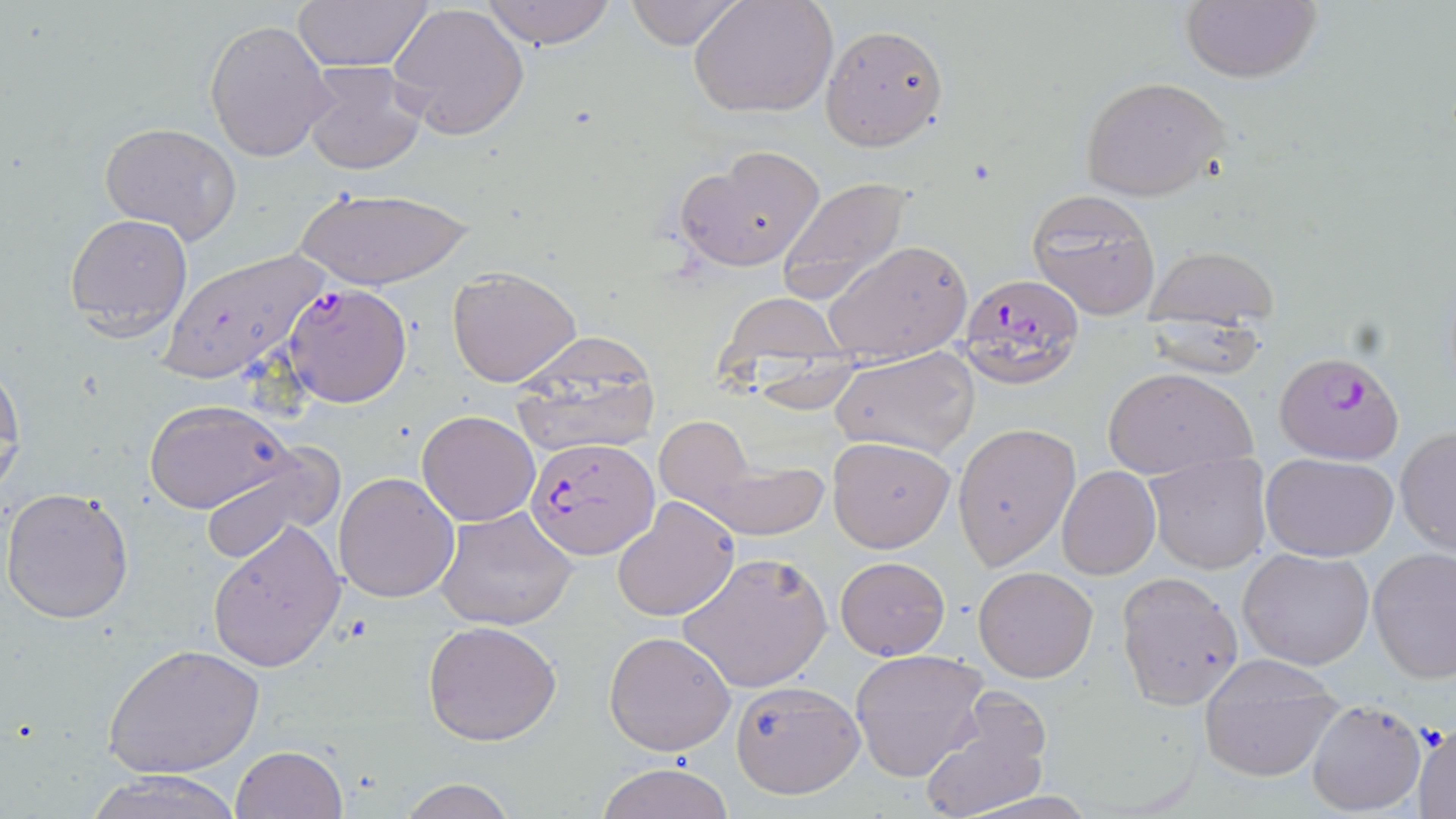

Summary:
  - Coordinate format: approximate bounding boxes as [x1, y1, x2, y2] in pixels
  - Plasmodium falciparum-infected red blood cell locations: [958, 270, 1086, 392], [283, 284, 412, 407], [1271, 356, 1408, 466], [525, 439, 657, 564]
  - Uninfected red blood cell locations: [476, 0, 619, 48], [621, 0, 748, 49], [688, 0, 838, 120], [292, 2, 437, 71], [388, 2, 531, 140], [1179, 2, 1320, 84], [204, 18, 336, 161], [820, 24, 950, 152], [301, 61, 428, 175], [1078, 76, 1229, 201], [99, 122, 242, 243], [676, 145, 827, 270], [777, 178, 911, 303], [292, 186, 475, 291], [1026, 186, 1165, 320], [65, 212, 194, 339], [824, 239, 972, 364], [1143, 241, 1279, 332], [158, 249, 334, 385], [446, 266, 583, 389], [715, 291, 850, 390], [512, 330, 663, 459], [829, 345, 979, 459], [0, 367, 24, 491], [1103, 367, 1255, 481], [144, 399, 294, 515], [416, 411, 539, 526], [652, 415, 752, 512], [953, 422, 1080, 568], [1396, 428, 1456, 554], [827, 435, 955, 552], [196, 446, 341, 565], [690, 448, 830, 542], [1145, 451, 1272, 573], [1261, 453, 1398, 561], [1057, 467, 1160, 579], [333, 472, 460, 603], [2, 487, 134, 625], [613, 496, 740, 623], [434, 506, 578, 632], [208, 520, 347, 671], [1368, 547, 1456, 683], [1238, 548, 1375, 671], [679, 551, 833, 695], [835, 556, 950, 659], [973, 566, 1097, 682], [1115, 570, 1245, 710], [423, 620, 563, 746], [603, 631, 735, 756], [103, 642, 264, 778], [850, 648, 988, 781], [1198, 657, 1343, 782], [729, 680, 865, 800], [919, 691, 1052, 819], [1306, 699, 1427, 815], [1413, 723, 1455, 817], [230, 746, 346, 819], [596, 762, 736, 819], [83, 769, 246, 819], [398, 777, 516, 819]
  - Slide-level diagnosis: Plasmodium falciparum
  - Preparation: thin blood film
  - Stain: May-Grünwald-Giemsa
  - Image size: 1456×819 pixels
  - Modality: optical microscopy
  - Field of view: one of a larger specimen
  - Magnification: 1000x